Describe the morphology of the red blood cells.
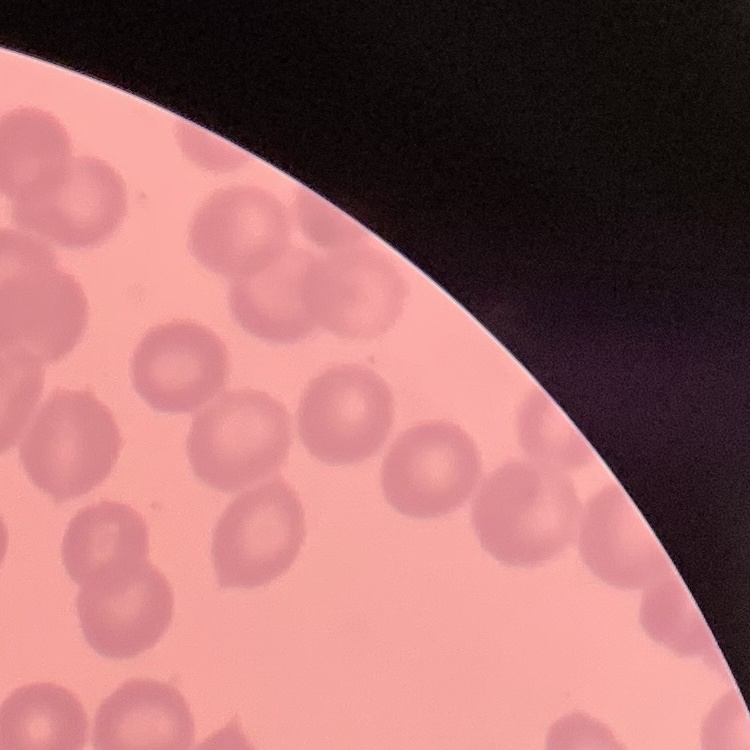

They show no rouleaux formation.

preparation = thin blood smear
stain = Field's or Giemsa
image type = one tile cut from a larger photomicrograph